Locate every Plasmodium ovale-infected red blood cell.
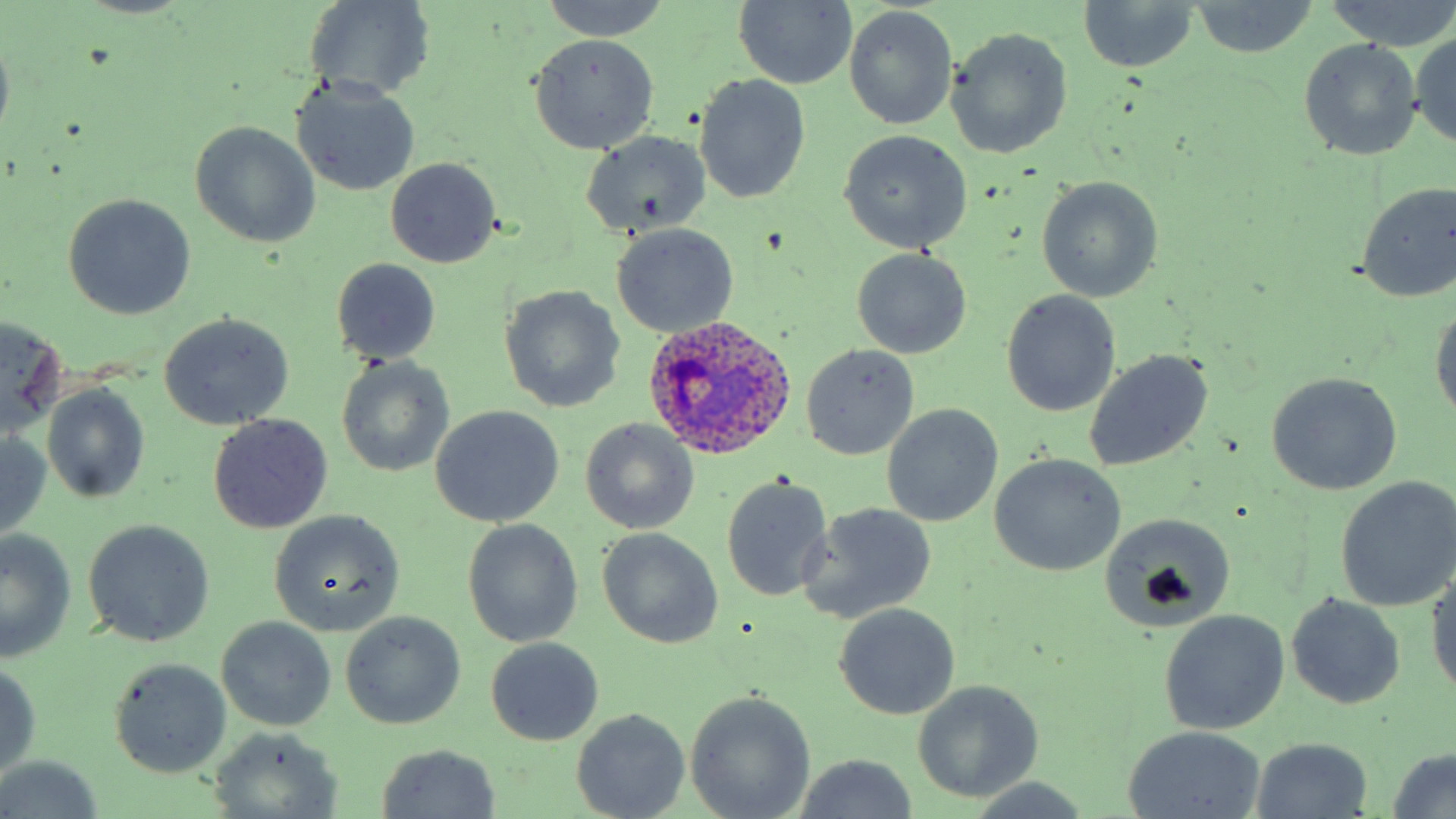
Approximate bounding boxes as (x1, y1, x2, y2) in pixels.
Plasmodium ovale-infected red blood cells: (644, 314, 797, 462).

Uninfected red blood cell locations: (539, 0, 673, 40), (1325, 0, 1456, 51), (304, 1, 436, 102), (732, 1, 857, 89), (1080, 2, 1200, 72), (1188, 2, 1319, 56), (843, 6, 957, 130), (947, 27, 1073, 159), (0, 30, 14, 143), (1409, 32, 1456, 148), (528, 33, 660, 154), (1298, 38, 1424, 161), (694, 74, 810, 203), (292, 80, 420, 196), (190, 121, 321, 249), (838, 129, 974, 253), (580, 131, 711, 240), (385, 158, 500, 269), (1036, 176, 1162, 303), (1354, 181, 1456, 303), (63, 194, 196, 319), (611, 224, 739, 338), (852, 249, 970, 358), (330, 258, 442, 364), (499, 284, 626, 413), (1001, 291, 1121, 417), (1429, 305, 1456, 427), (158, 313, 295, 430), (1, 315, 67, 437), (801, 344, 918, 459), (1085, 349, 1214, 471), (336, 356, 454, 479), (1265, 373, 1402, 496), (41, 383, 151, 506), (881, 404, 1002, 527), (431, 406, 564, 527), (209, 414, 331, 533), (581, 418, 700, 534), (0, 433, 52, 538), (990, 453, 1126, 576), (720, 475, 834, 602), (1334, 477, 1456, 611), (799, 506, 937, 626), (1098, 509, 1236, 630), (269, 510, 405, 636), (83, 519, 214, 647), (461, 519, 584, 648), (596, 527, 724, 650), (0, 531, 78, 661), (1426, 566, 1456, 700), (1286, 593, 1405, 709), (833, 603, 961, 720), (340, 610, 465, 729), (1159, 610, 1290, 736), (217, 617, 336, 731), (486, 637, 602, 745), (109, 658, 232, 778), (0, 660, 43, 776), (911, 681, 1045, 803), (685, 692, 816, 819), (572, 707, 690, 819), (1120, 725, 1266, 819), (210, 729, 342, 815), (1249, 737, 1374, 818), (375, 744, 502, 819), (1385, 747, 1456, 819), (793, 755, 918, 819), (0, 760, 107, 818), (967, 777, 1097, 819). Slide-level diagnosis: Plasmodium ovale. May-Grünwald-Giemsa stain. Captured at 1000x magnification. Thin blood smear. One field of a larger specimen. Light microscopy. Image is 1456×819 pixels.